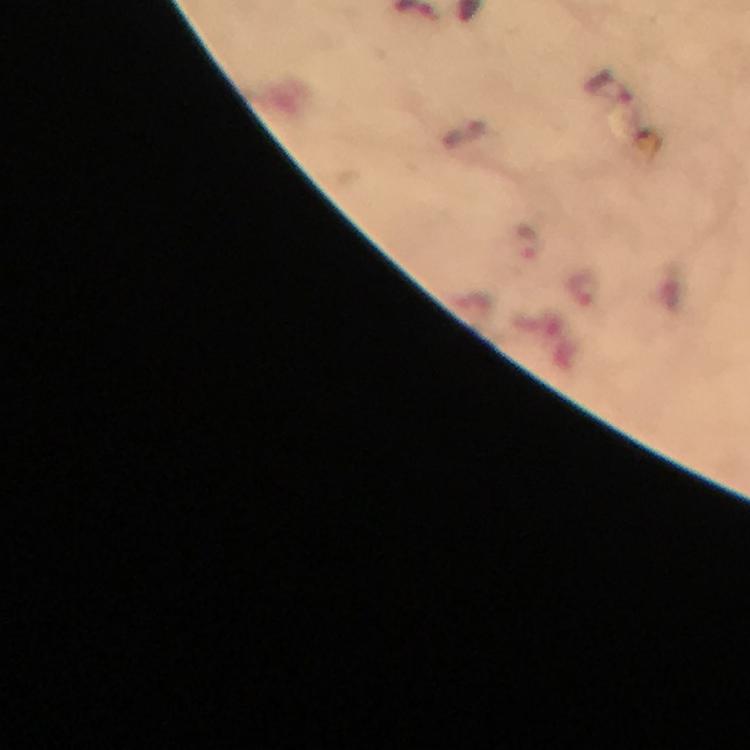 Approximate centers as (x, y) in pixels. Plasmodium parasite locations: (610, 88), (524, 245). Thick blood smear. At 100x magnification. Image is 750×750 pixels. From a malaria diagnostic workup. Immersion oil was used. A crop from one field of view. Giemsa stain. Smartphone photograph taken through a microscope.